Comment on the morphology of the red blood cells.
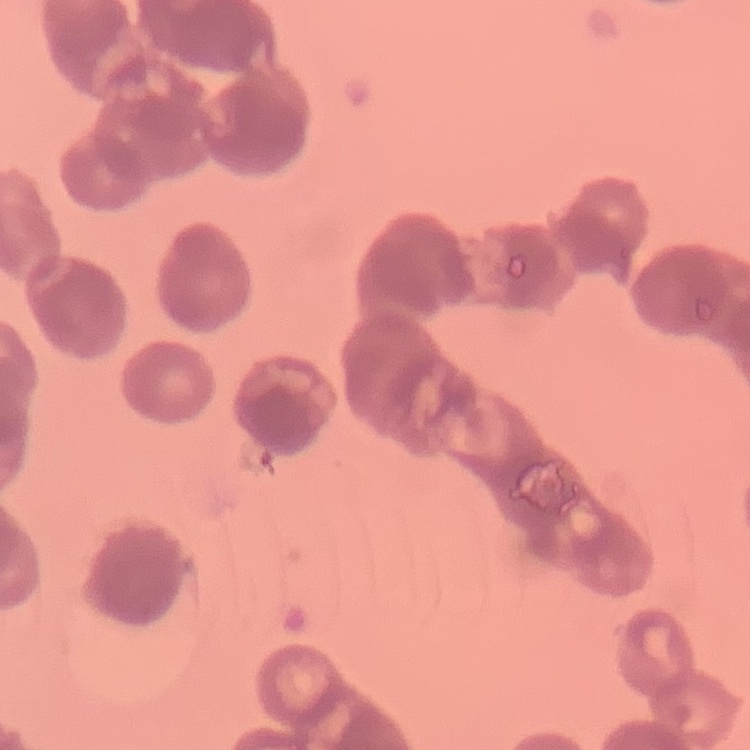

They show rouleaux formation.

Summary:
  - Stain: Field's or Giemsa
  - Preparation: thin peripheral smear
  - Image type: one tile cut from a larger photomicrograph